Assess this cell for malaria.
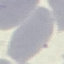

Uninfected.

Cell patch, automatically extracted from a larger field of view and resized to 64 × 64 pixels. Giemsa-stained preparation. Thin blood film. Photographed with a smartphone camera at the microscope eyepiece.